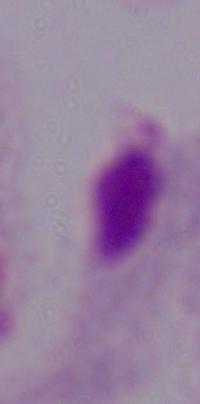

Summary:
  - Modality: photomicrograph
  - Identification: trichomonad
  - Magnification: 1000x